Identify the preparation type.
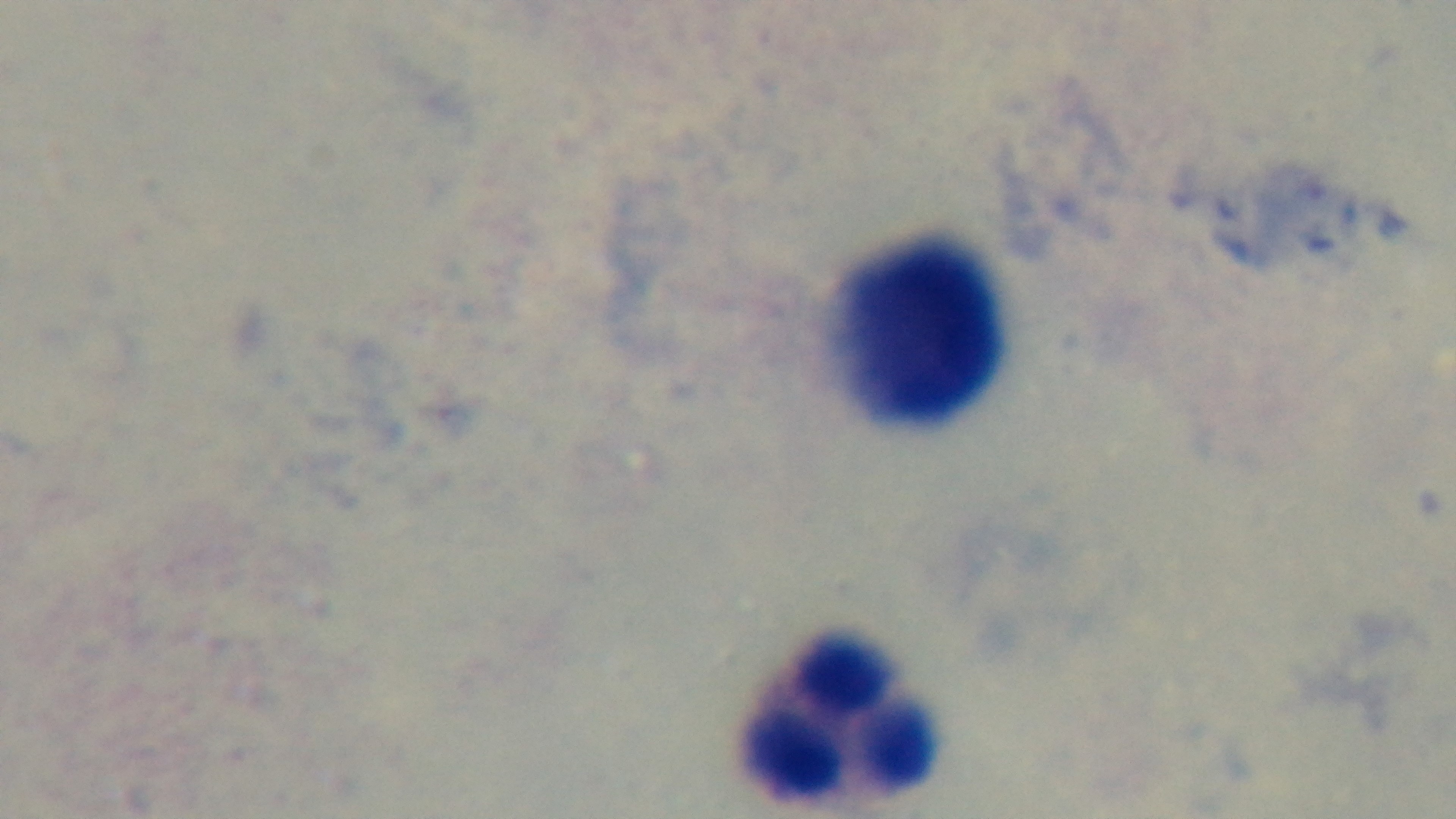
A thick smear.

Malaria status: uninfected. Light microscopy. Single field of view. Mounted 4K digital camera. Giemsa-stained. 100x oil-immersion objective.